Identify the parasite.
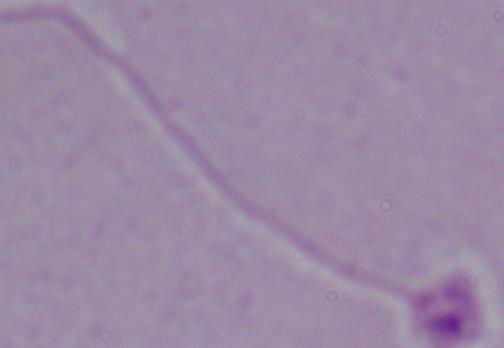

Leishmania.

1000x magnification. Photomicrograph.